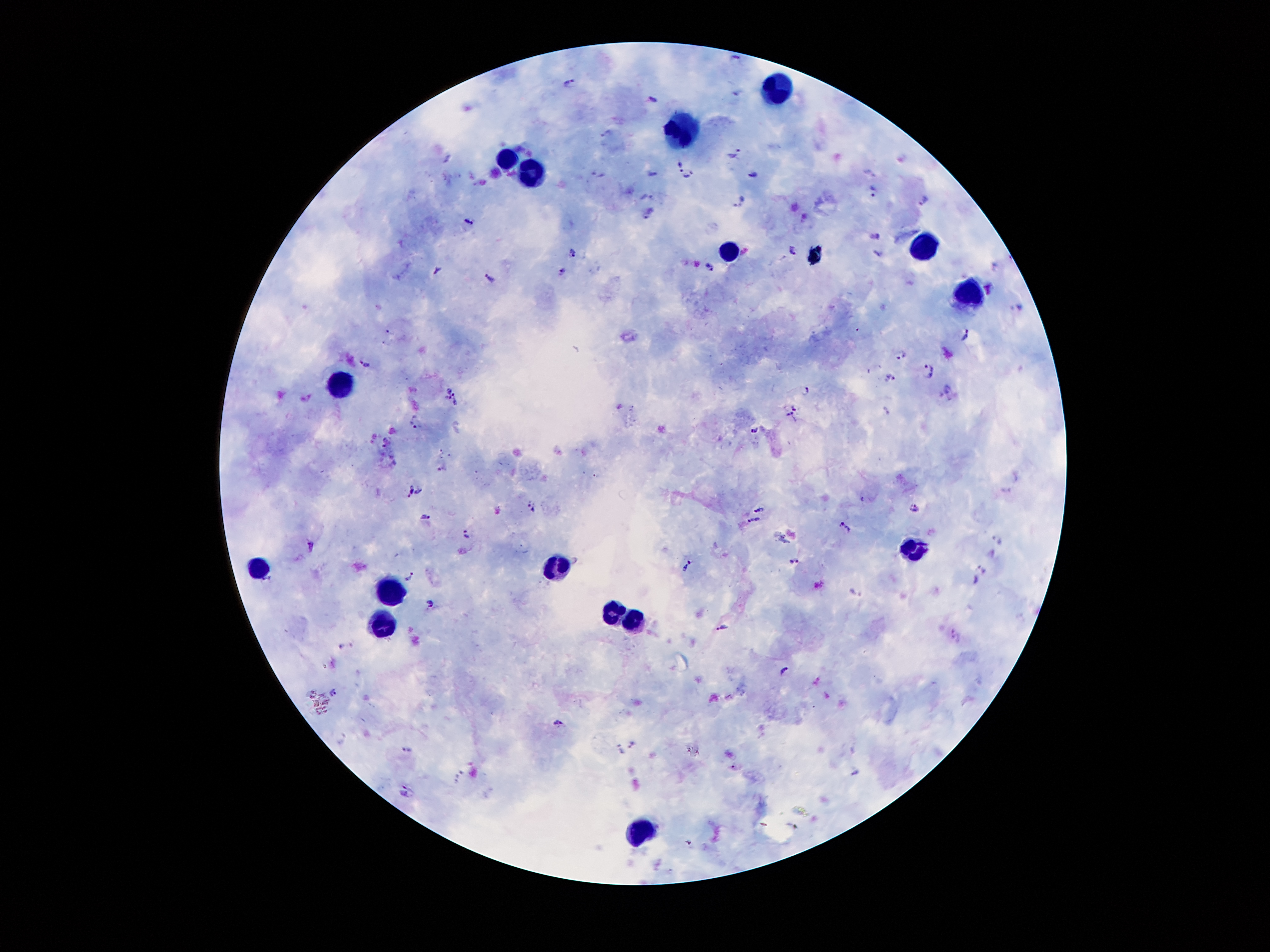

Approximate object centers, in pixels from the top-left corner.
Summary:
  - Leukocyte locations: (x=782, y=88), (x=686, y=136), (x=503, y=157), (x=538, y=175), (x=922, y=245), (x=731, y=251), (x=971, y=294), (x=350, y=386), (x=914, y=553), (x=554, y=561), (x=265, y=571), (x=389, y=589), (x=612, y=606), (x=638, y=616), (x=385, y=621), (x=641, y=824)
  - Malaria parasite locations: (x=736, y=56), (x=570, y=84), (x=737, y=92), (x=649, y=97), (x=735, y=154), (x=903, y=157), (x=679, y=162), (x=870, y=170), (x=752, y=171), (x=654, y=174), (x=691, y=175), (x=875, y=193), (x=645, y=196), (x=742, y=200), (x=925, y=200), (x=793, y=204), (x=648, y=212), (x=805, y=215), (x=469, y=221), (x=875, y=237), (x=791, y=249), (x=574, y=254), (x=878, y=255), (x=995, y=264), (x=711, y=267), (x=438, y=271), (x=560, y=274), (x=490, y=279), (x=988, y=288), (x=1020, y=308), (x=967, y=334), (x=901, y=354), (x=365, y=364), (x=929, y=371), (x=892, y=378), (x=947, y=388), (x=806, y=391), (x=445, y=393), (x=458, y=397), (x=795, y=404), (x=886, y=411), (x=789, y=417), (x=415, y=422), (x=754, y=431), (x=383, y=442), (x=442, y=467), (x=408, y=491), (x=419, y=491), (x=1005, y=492), (x=531, y=507), (x=759, y=507), (x=914, y=507), (x=426, y=515), (x=753, y=521), (x=840, y=522), (x=850, y=529), (x=466, y=534), (x=998, y=541), (x=311, y=545), (x=794, y=561), (x=686, y=567), (x=982, y=569), (x=410, y=578), (x=975, y=582), (x=855, y=593), (x=431, y=602), (x=723, y=626), (x=952, y=631), (x=340, y=646), (x=785, y=670), (x=333, y=693), (x=558, y=724), (x=632, y=744), (x=407, y=751), (x=621, y=751), (x=857, y=772), (x=405, y=791)
  - Field of view: one from this slide
  - Stain: Giemsa
  - Magnification: 100x
  - Preparation: thick blood smear
  - Patient malaria status: positive for Plasmodium falciparum
  - Capture: smartphone through the microscope eyepiece
  - Image size: 1270×952 pixels